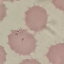

result: no malaria parasites seen
preparation: thin smear
stain: Giemsa
image_type: automatically extracted cell patch, resized to 64 × 64 pixels
capture: smartphone through the microscope eyepiece